Give the position of every Plasmodium parasite visible.
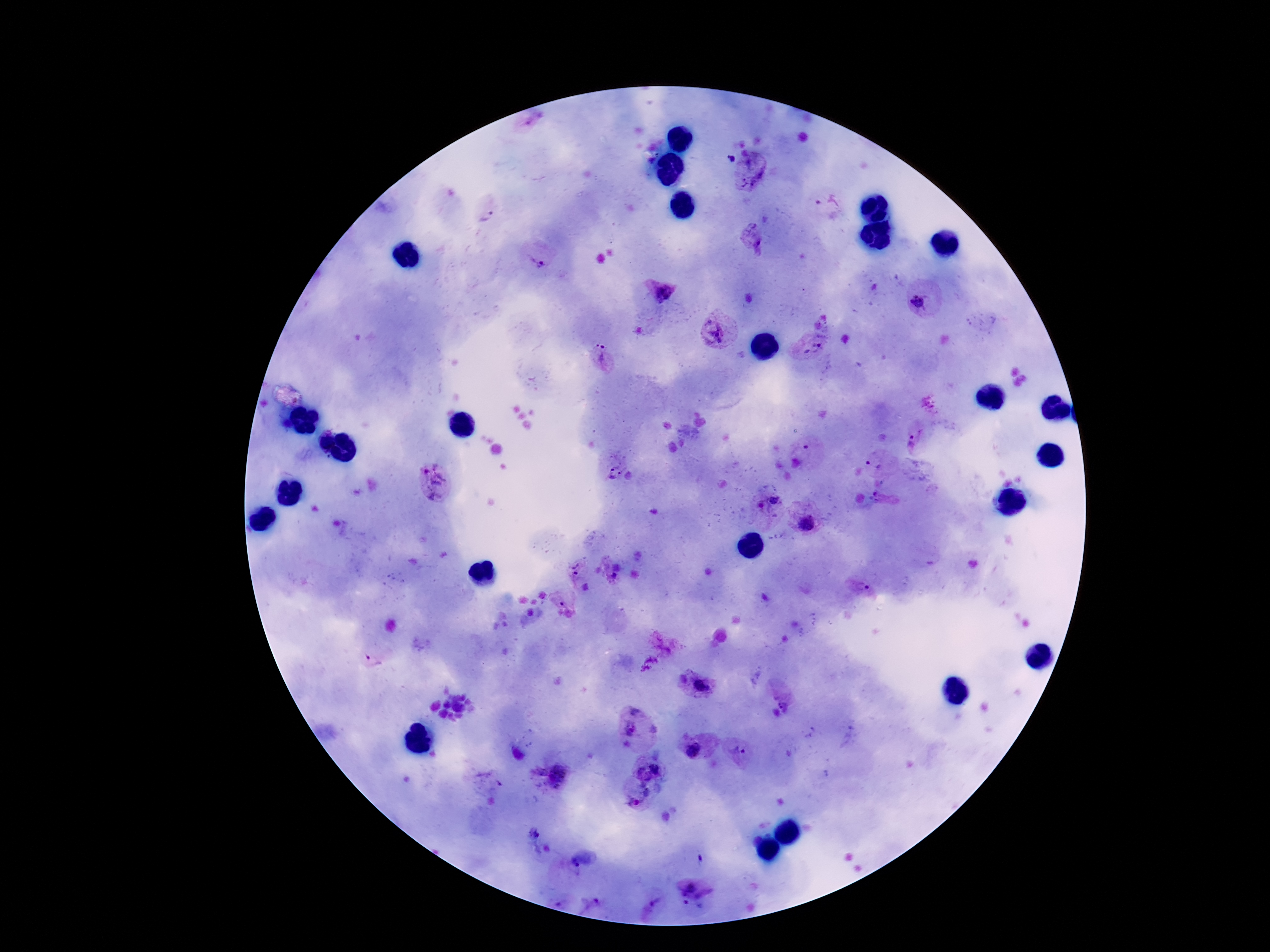

Approximate centers as (x, y) in pixels.
Plasmodium parasites: (533, 121), (732, 159), (751, 173), (828, 202), (488, 215), (754, 241), (538, 261), (660, 290), (921, 302), (718, 331), (816, 341), (604, 355), (928, 402), (913, 439), (808, 447), (873, 465), (615, 468), (433, 482), (875, 494), (880, 500), (761, 505), (807, 523), (578, 569), (613, 577), (862, 587), (561, 604), (530, 612), (665, 647), (373, 662), (682, 680), (703, 687), (785, 703), (637, 730), (846, 737), (692, 750), (739, 752), (655, 769), (641, 772), (538, 773), (566, 779), (649, 780), (491, 781), (646, 793), (634, 802), (535, 834), (700, 858), (580, 859), (684, 887), (707, 899), (656, 902), (558, 903), (591, 903), (687, 904).

capture = smartphone camera through the microscope eyepiece
field of view = one from this slide
patient malaria status = infected
magnification = 100x
preparation = thick blood film
image size = 1270×952 pixels
stain = Giemsa